Identify the blood parasite species.
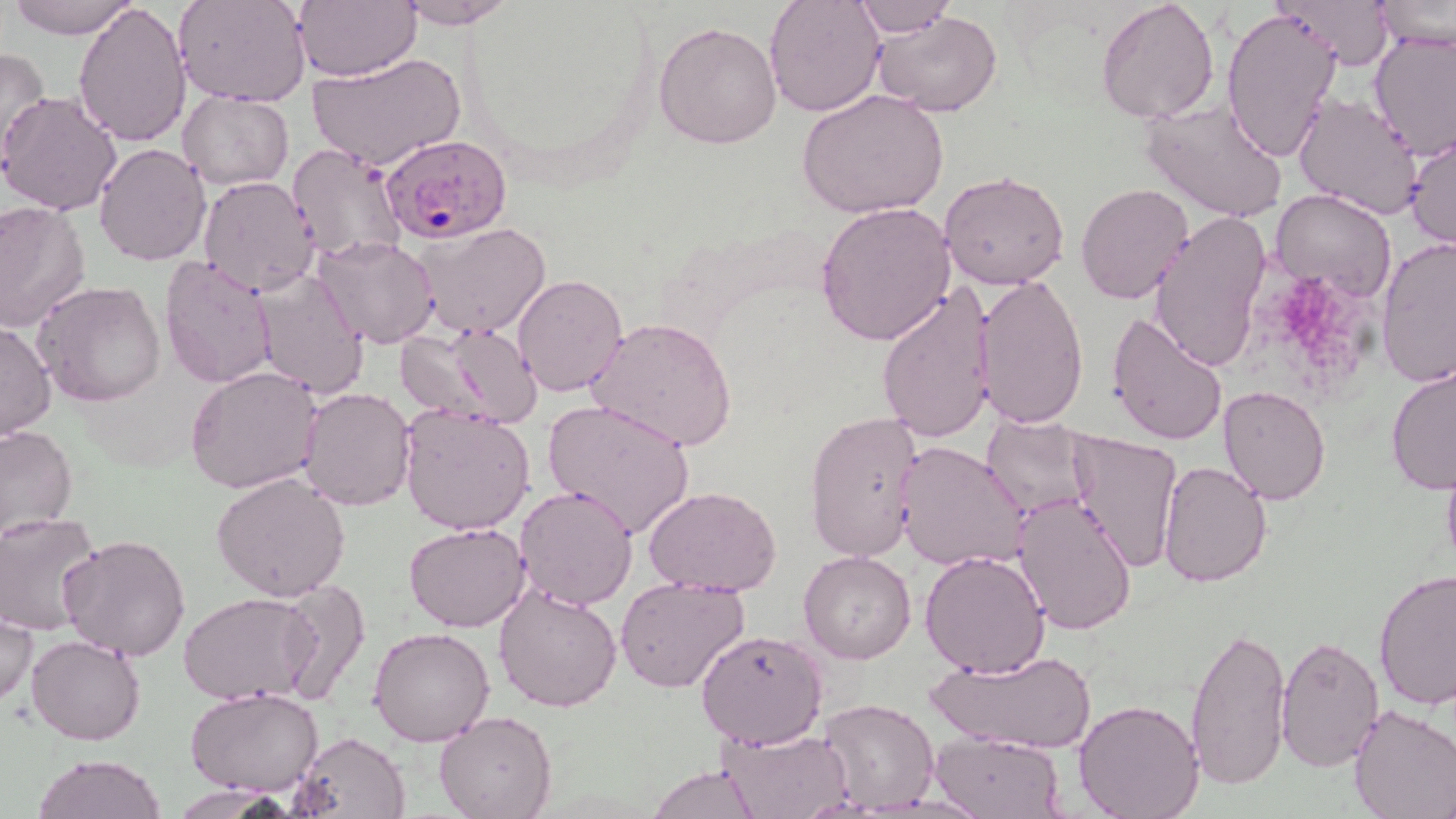

Plasmodium falciparum.

field of view = one of a larger specimen
platelet locations = approximate bounding boxes as (x1,y1)-(x2,y2) corner pairs in pixels: (1284,285)-(1349,358)
stain = May-Grünwald-Giemsa
Plasmodium falciparum-infected red blood cell locations = approximate bounding boxes as (x1,y1)-(x2,y2) corner pairs in pixels: (380,132)-(513,245)
magnification = 1000x
uninfected red blood cell locations = approximate bounding boxes as (x1,y1)-(x2,y2) corner pairs in pixels: (9,0)-(139,39), (173,0)-(313,106), (293,0)-(420,81), (393,0)-(518,29), (763,0)-(886,117), (855,0)-(956,38), (1096,0)-(1220,122), (1378,0)-(1455,52), (74,1)-(192,147), (1280,1)-(1394,69), (1221,6)-(1342,164), (871,10)-(1003,116), (653,22)-(782,149), (1369,32)-(1455,158), (0,46)-(51,168), (309,52)-(465,171), (797,88)-(948,218), (0,90)-(123,215), (177,90)-(293,190), (1293,94)-(1424,221), (1139,98)-(1289,222), (1405,132)-(1455,250), (94,143)-(211,265), (287,144)-(409,266), (938,170)-(1069,290), (197,177)-(324,297), (1076,182)-(1194,304), (1271,189)-(1398,304), (0,199)-(91,332), (814,200)-(955,345), (1147,211)-(1273,373), (412,220)-(554,338), (1375,235)-(1456,386), (314,236)-(438,349), (159,255)-(277,389), (250,267)-(370,400), (974,273)-(1090,430), (512,275)-(627,396), (34,281)-(168,407), (877,282)-(1001,447), (1105,311)-(1230,447), (587,315)-(738,452), (0,321)-(56,441), (398,323)-(545,429), (1385,359)-(1456,495), (186,367)-(322,494), (1218,385)-(1331,505), (298,389)-(417,511), (543,397)-(697,540), (398,403)-(536,536), (806,410)-(926,564), (981,416)-(1097,518), (0,422)-(77,538), (1065,429)-(1183,573), (897,441)-(1027,573), (1440,444)-(1456,580), (1156,461)-(1274,588), (211,472)-(351,601), (515,483)-(638,611), (645,485)-(782,597), (1009,492)-(1139,635), (0,513)-(103,634), (404,523)-(531,633), (58,531)-(192,662), (798,550)-(916,664), (920,550)-(1051,678), (1372,566)-(1455,710), (614,577)-(750,693), (274,581)-(372,707), (494,584)-(623,714), (178,592)-(320,705), (0,608)-(38,709), (1185,622)-(1292,793), (369,628)-(496,746), (696,628)-(828,750), (27,634)-(145,746), (1275,636)-(1384,769), (926,647)-(1095,756), (186,687)-(325,797), (817,697)-(938,815), (1072,699)-(1205,819), (1347,704)-(1456,819), (434,711)-(558,819), (717,726)-(855,818), (291,730)-(411,818), (930,731)-(1064,818), (32,754)-(169,819), (648,764)-(761,819)
modality = light microscopy
preparation = thin blood film
image size = 1456×819 pixels